Assess this cell for malaria.
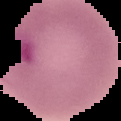

Parasitized.

image size = 121×121 pixels
image type = segmented cell region on a black background
preparation = thin blood film